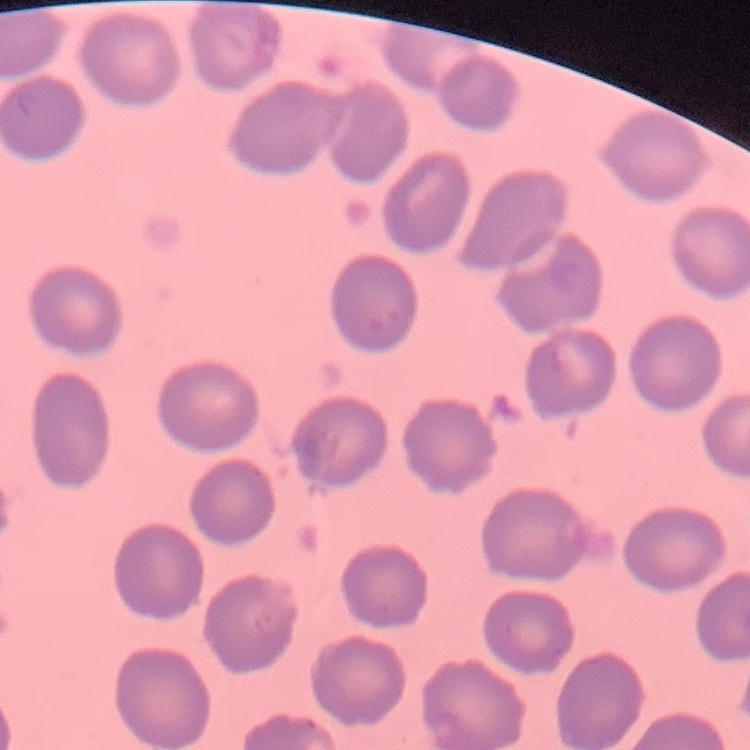
erythrocyte morphology = no rouleaux formation
image type = square crop of a larger photomicrograph
preparation = thin blood film
stain = Field's or Giemsa